Report the malaria status of this cell.
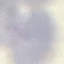
Uninfected.

preparation: thin blood film
image_type: cell patch, automatically extracted from a larger field of view and resized to 64 × 64 pixels
stain: Giemsa
capture: smartphone through the microscope eyepiece